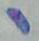
identification: Toxoplasma gondii
magnification: 1000x
modality: photomicrograph